Mark where platelets are.
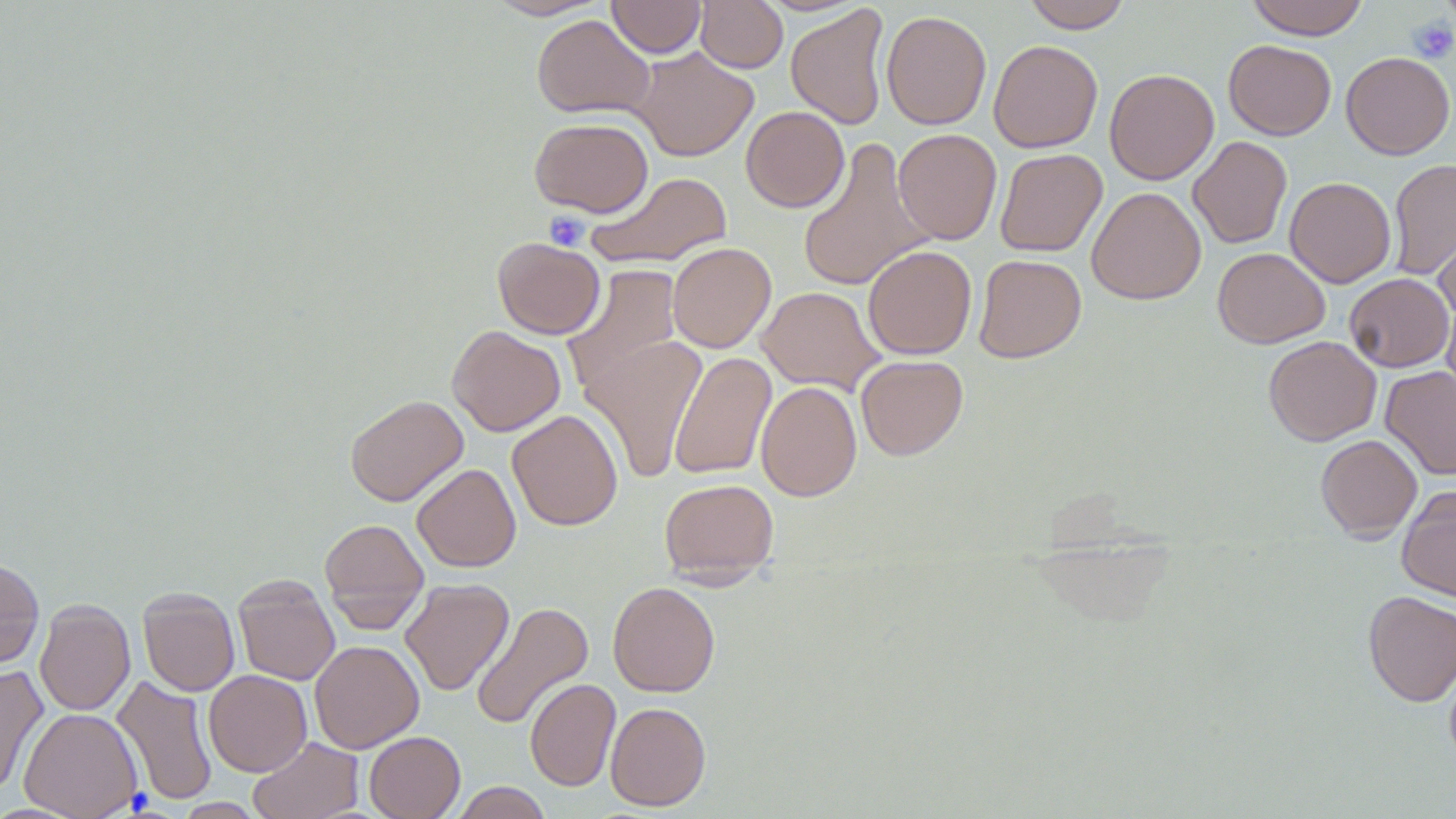
Approximate bounding boxes as (x1,y1)-(x2,y2) corner pairs in pixels.
Platelets: (1409,18)-(1456,63), (544,210)-(590,251).

Summary:
  - Uninfected red blood cell locations: (486,0)-(610,20), (607,0)-(706,58), (695,0)-(787,73), (1022,0)-(1132,32), (1246,0)-(1369,39), (786,4)-(891,130), (881,9)-(992,130), (532,14)-(655,119), (1223,39)-(1336,140), (988,40)-(1103,153), (631,47)-(759,161), (1341,52)-(1455,159), (1104,68)-(1219,185), (741,106)-(849,212), (530,117)-(653,217), (892,128)-(1002,245), (1187,136)-(1292,249), (797,138)-(932,293), (995,148)-(1107,257), (1387,158)-(1456,280), (586,172)-(733,269), (1284,176)-(1396,288), (1086,187)-(1206,304), (1432,216)-(1456,324), (493,238)-(605,339), (667,242)-(776,353), (862,245)-(977,360), (1212,247)-(1329,348), (973,254)-(1087,363), (563,264)-(683,392), (1344,273)-(1453,372), (756,286)-(885,396), (1442,295)-(1456,400), (447,325)-(565,436), (578,333)-(708,482), (1263,335)-(1381,446), (669,351)-(776,481), (855,354)-(968,460), (1380,366)-(1456,480), (756,380)-(862,501), (345,394)-(468,507), (507,409)-(623,531), (1315,434)-(1423,541), (411,463)-(521,572), (659,478)-(779,583), (1397,486)-(1456,601), (318,517)-(430,631), (0,557)-(44,670), (233,574)-(340,686), (400,578)-(514,696), (607,581)-(720,697), (138,587)-(240,696), (1362,590)-(1456,706), (34,599)-(135,716), (471,601)-(594,730), (309,640)-(424,753), (1444,658)-(1456,769), (0,664)-(48,796), (204,670)-(312,776), (112,674)-(218,806), (525,678)-(620,791), (605,701)-(711,811), (20,707)-(143,818), (364,731)-(465,819), (249,737)-(364,819), (450,782)-(553,818), (173,797)-(265,818)
  - Slide-level diagnosis: negative for blood parasites
  - Image size: 1456×819 pixels
  - Field of view: one of a larger specimen
  - Magnification: 1000x
  - Modality: light microscopy
  - Preparation: thin blood film
  - Stain: May-Grünwald-Giemsa